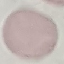

Result: no malaria parasites detected. Thin smear of blood. Cell patch, automatically extracted from a larger field of view and resized to 64 × 64 pixels. Photographed with a smartphone camera at the microscope eyepiece. Giemsa stain.